Report the malaria status of this cell.
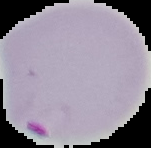

Parasitized.

Image is 151×148 pixels. From a thin blood smear. Cell region segmented out of the field of view; the surrounding area is masked to black.